Point out each Plasmodium parasite.
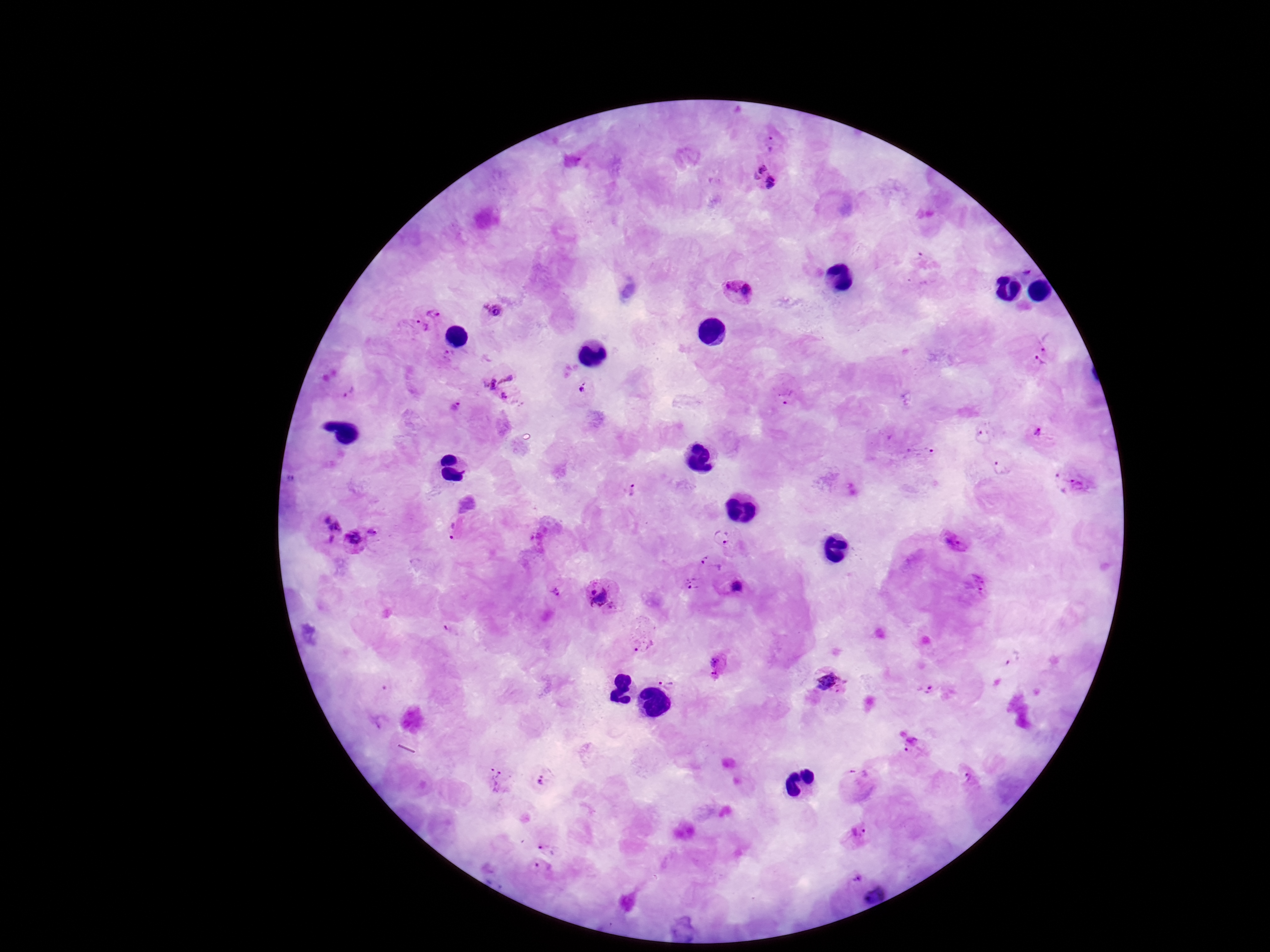

Approximate centers as (x, y) in pixels.
Plasmodium parasites: (772, 141), (766, 178), (739, 291), (435, 310), (493, 311), (418, 330), (1034, 353), (495, 372), (584, 388), (347, 389), (786, 394), (510, 397), (457, 407), (985, 433), (1037, 438), (918, 452), (999, 466), (1074, 484), (633, 492), (327, 523), (376, 531), (455, 531), (722, 535), (953, 539), (354, 541), (710, 565), (730, 583), (975, 585), (691, 587), (554, 596), (604, 598), (454, 626), (644, 633), (1013, 657), (721, 666), (672, 680), (830, 683), (928, 690), (910, 742), (499, 780), (543, 780), (969, 781), (859, 783), (857, 835), (549, 842), (538, 875), (855, 879), (876, 894).

stain = Giemsa
magnification = 100x
capture = smartphone camera through the microscope eyepiece
image size = 1270×952 pixels
preparation = thick blood film
patient malaria status = positive
field of view = one from this slide